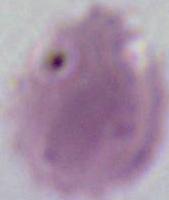

Micrograph. An erythrocyte is seen. 1000x magnification.